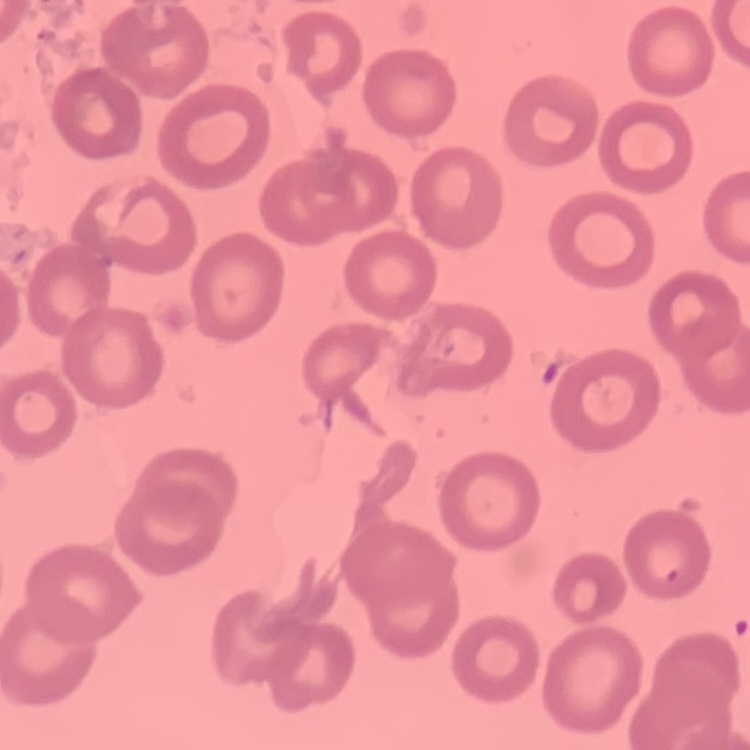

Summary:
  - Erythrocyte morphology: no rouleaux formation
  - Image type: square crop of a larger photomicrograph
  - Preparation: thin peripheral smear
  - Stain: Field's or Giemsa